Assess this cell for malaria.
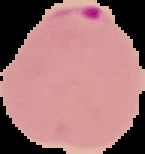
Parasitized.

Summary:
  - Image size: 145×154 pixels
  - Image type: cell region segmented out of the field of view; surrounding area masked to black
  - Preparation: thin blood smear